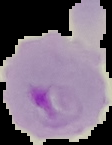 Result: malaria parasites detected. Image is 112×145 pixels. From a thin blood smear. The area outside the segmented cell region is set to black.